Identify the preparation type.
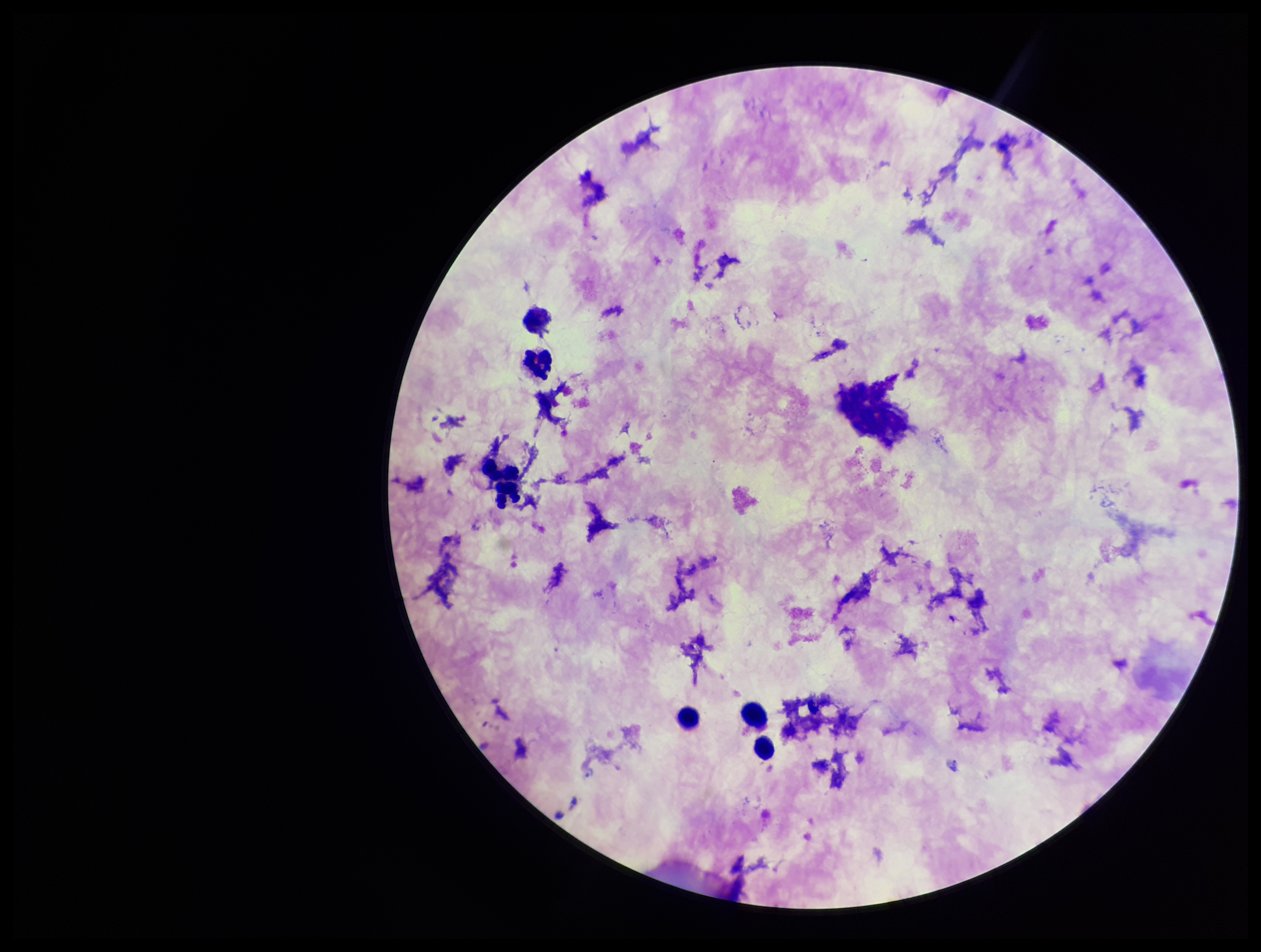

Thick.

Summary:
  - Patient malaria status: positive
  - Capture: smartphone photograph through the microscope eyepiece
  - Parasite count: 0
  - Stain: Giemsa
  - Leukocyte count: 6
  - Species reported for this patient: Plasmodium falciparum
  - Image size: 1261×952 pixels
  - Plasmodium parasites: none seen
  - Field of view: one from this slide